Name the blood parasite species.
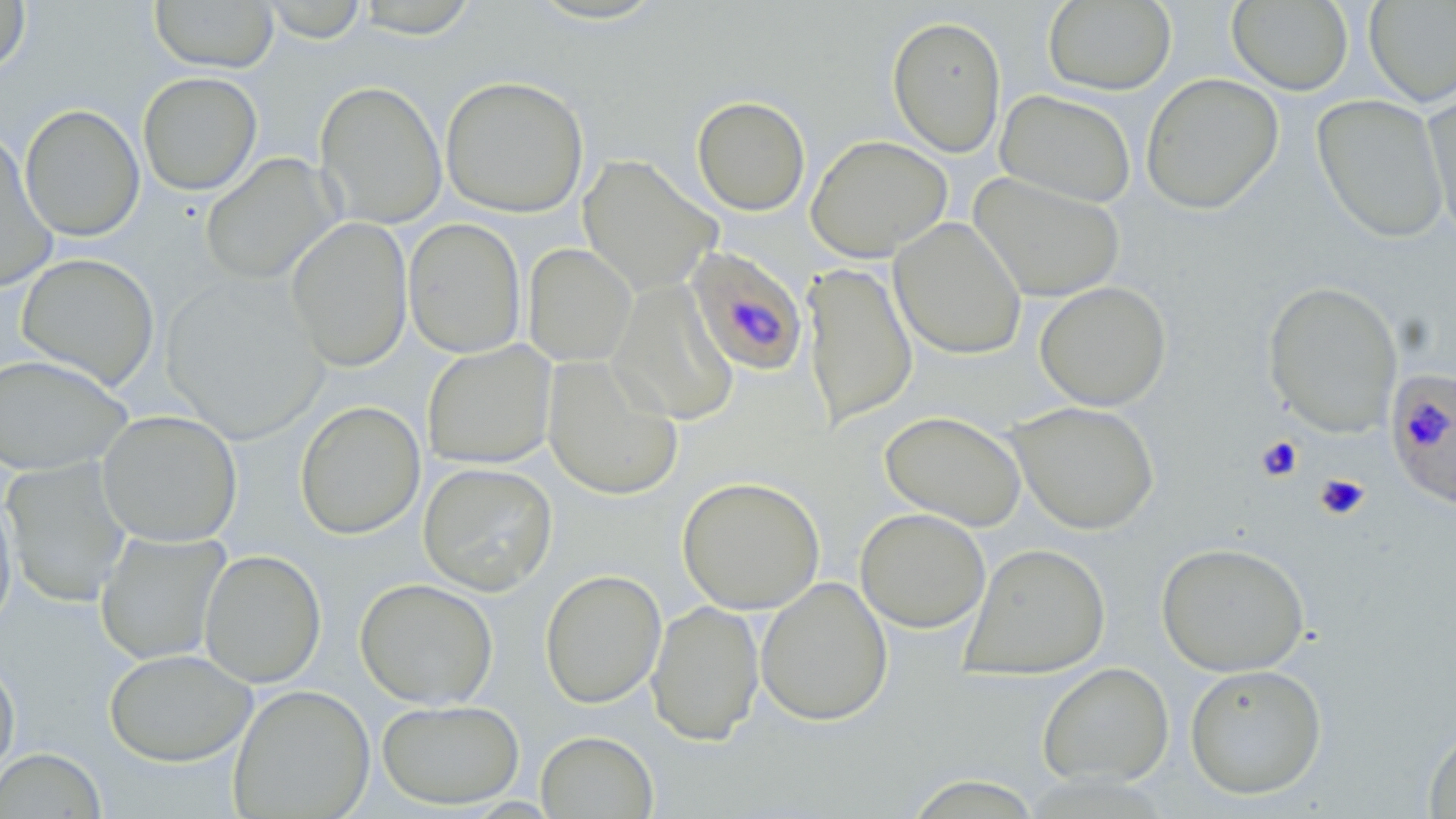
Plasmodium falciparum.

{
  "field_of_view": "one of a larger specimen",
  "modality": "optical microscopy",
  "uninfected_red_blood_cell_locations": "approximate bounding boxes as (x1, y1, x2, y2) in pixels: (150, 0, 279, 72), (260, 0, 368, 43), (352, 0, 480, 38), (520, 0, 674, 26), (1363, 0, 1456, 107), (0, 1, 31, 75), (1042, 1, 1177, 95), (1227, 1, 1353, 95), (887, 15, 1006, 157), (137, 72, 262, 196), (1141, 73, 1284, 215), (440, 76, 589, 218), (315, 80, 447, 229), (1421, 84, 1456, 245), (995, 89, 1137, 208), (1312, 94, 1450, 243), (691, 95, 811, 216), (20, 104, 145, 241), (805, 134, 953, 262), (0, 135, 58, 292), (200, 153, 339, 286), (578, 154, 723, 296), (968, 172, 1126, 302), (286, 217, 413, 372), (889, 217, 1027, 360), (404, 218, 526, 358), (523, 243, 636, 368), (16, 253, 160, 391), (802, 261, 917, 428), (160, 274, 330, 444), (1262, 280, 1403, 438), (1034, 281, 1171, 411), (609, 283, 739, 426), (422, 341, 556, 469), (0, 354, 133, 476), (542, 355, 684, 501), (294, 400, 426, 540), (1008, 401, 1161, 535), (97, 410, 243, 547), (879, 410, 1026, 530), (2, 459, 132, 607), (418, 462, 557, 596), (676, 476, 826, 614), (0, 488, 17, 633), (855, 507, 991, 633), (95, 531, 230, 665), (1156, 541, 1310, 676), (959, 542, 1111, 680), (199, 549, 326, 688), (539, 569, 667, 708), (755, 576, 893, 726), (355, 578, 499, 709), (646, 600, 765, 745), (104, 648, 256, 766), (0, 657, 20, 781), (1037, 662, 1174, 788), (1184, 663, 1327, 800), (228, 684, 375, 819), (377, 699, 525, 809), (1423, 725, 1456, 818), (536, 731, 658, 819), (0, 748, 107, 818)",
  "preparation": "thin blood film",
  "plasmodium_falciparum_infected_red_blood_cell_locations": "approximate bounding boxes as (x1, y1, x2, y2) in pixels: (685, 245, 808, 377), (1385, 369, 1456, 510)",
  "stain": "May-Grünwald-Giemsa",
  "image_size": "1456×819 pixels",
  "magnification": "1000x"
}